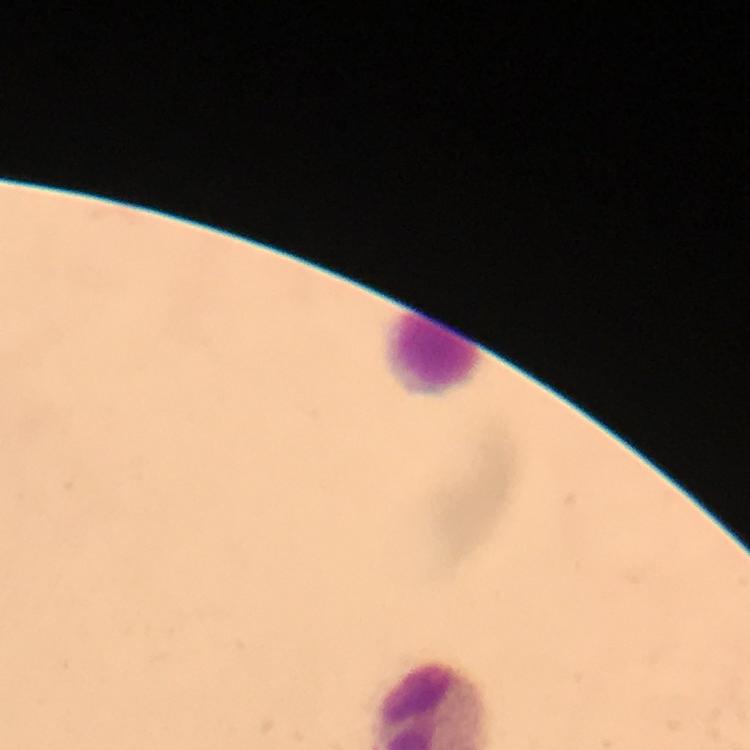
Approximate centers as [x, y] in pixels.
Summary:
  - Leukocyte locations: [435, 356]
  - Cropped from: one field of view
  - Preparation: thick blood film
  - Immersion oil: applied
  - Magnification: 100x
  - Malaria parasites: none detected
  - Capture: smartphone photograph through a microscope
  - Image size: 750×750 pixels
  - Context: from a diagnostic examination for malaria
  - Stain: Giemsa